State which parasite is depicted.
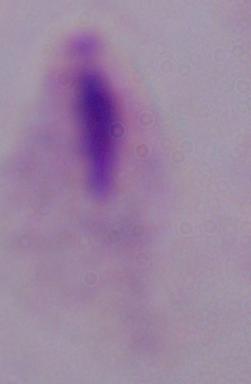

This is a trichomonad.

Captured at 1000x magnification. Micrograph.